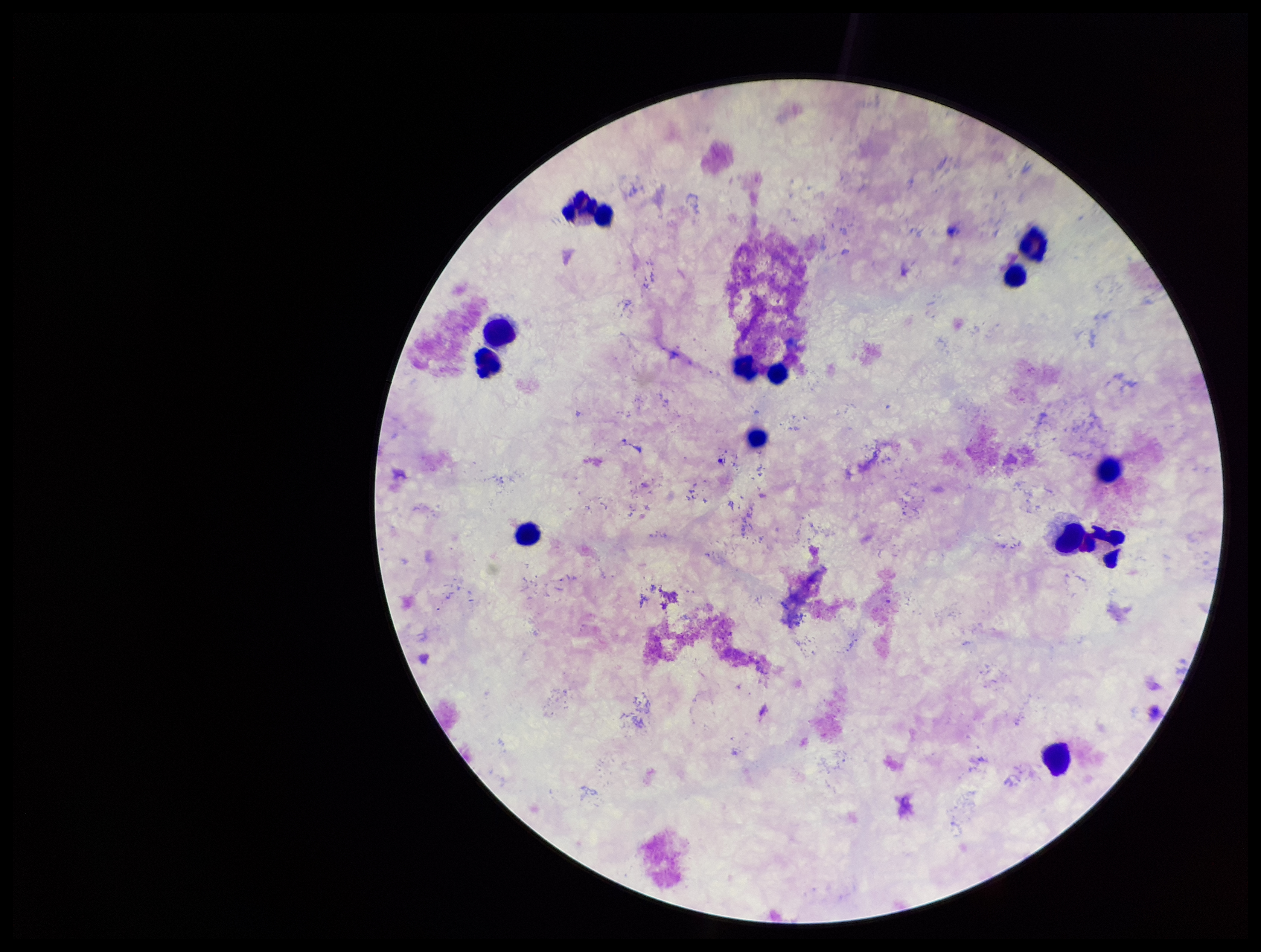 Giemsa stain. Preparation: thick blood smear. Parasite count: 0. Image is 1261×952 pixels. Plasmodium parasites: none seen. Leukocyte count: 13. Smartphone photograph taken through the eyepiece of a microscope. Patient malaria status: negative. One field from this slide.